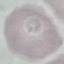

Summary:
  - Result: negative for malaria parasites
  - Image type: cell patch, automatically extracted from a larger field of view and resized to 64 × 64 pixels
  - Stain: Giemsa
  - Capture: smartphone through the microscope eyepiece
  - Preparation: thin smear